Identify the cell.
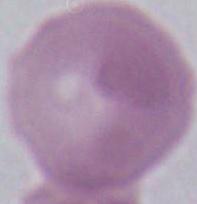
An erythrocyte.

magnification: 1000x
modality: photomicrograph